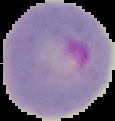
malaria_status: parasitized
preparation: thin blood film
image_type: segmented cell region with the area outside set to black
image_size: 115×121 pixels